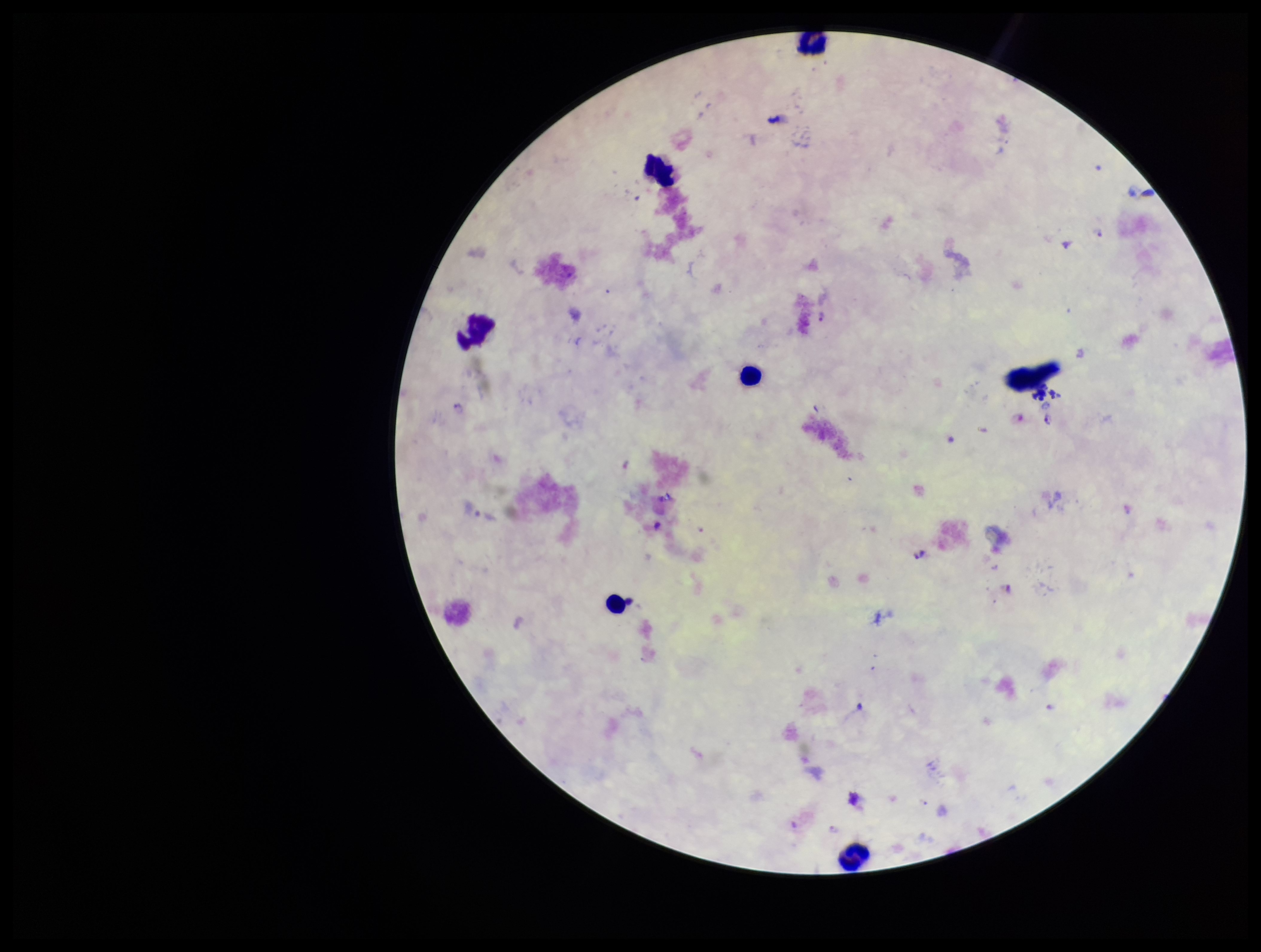
Leukocyte count: 6. Species reported for this patient: Plasmodium falciparum. Stained with Giemsa. Smartphone photograph taken through the eyepiece of a microscope. Plasmodium parasites: detected. One field from this slide. Preparation: thick smear. Parasite count: 5. Patient malaria status: positive. Image is 1261×952 pixels.